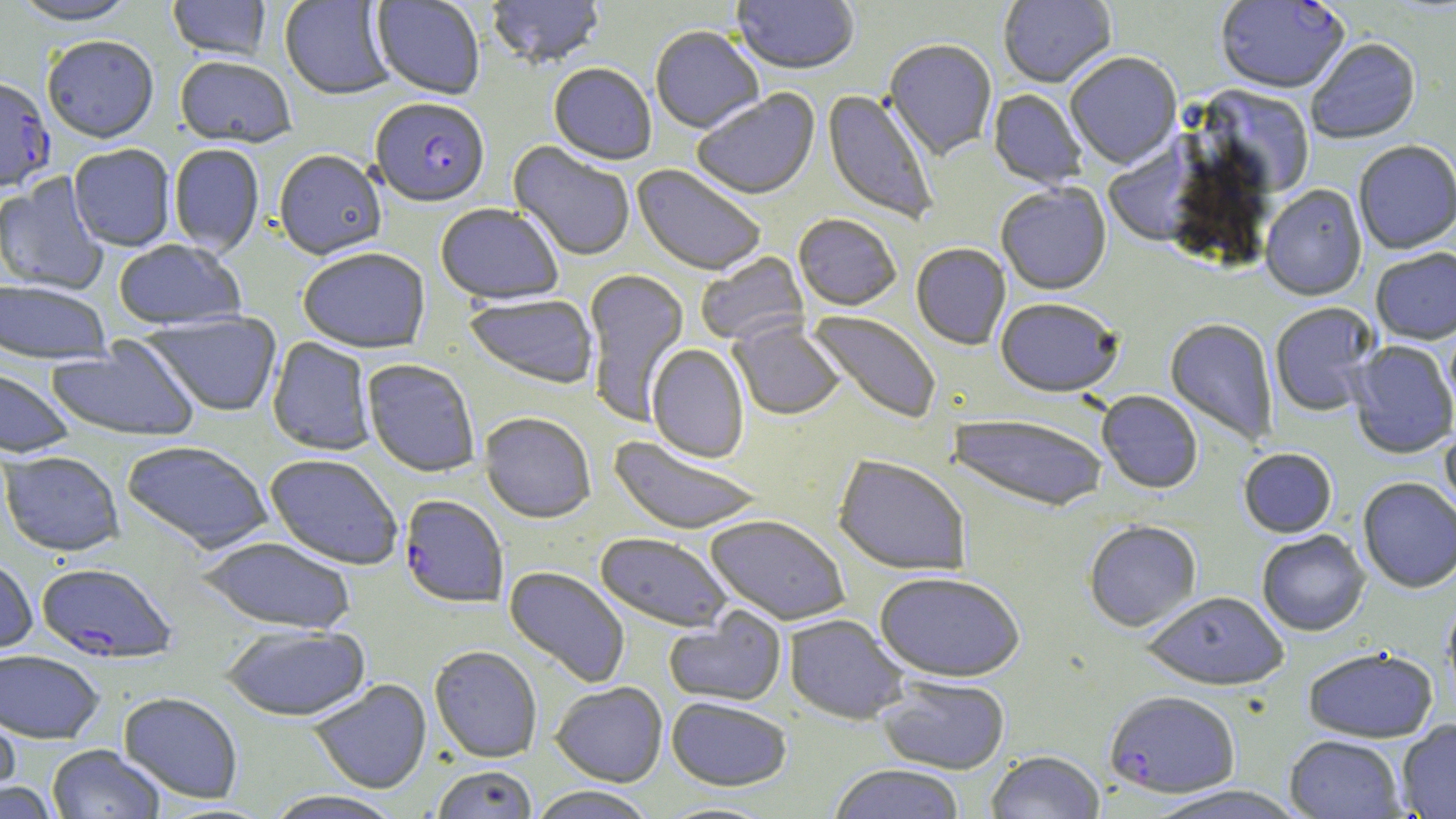

slide-level diagnosis = Plasmodium falciparum
field of view = one of a larger specimen
magnification = 1000x
preparation = thin blood film
uninfected red blood cell locations = approximate bounding boxes as [x1, y1, x2, y2] in pixels: [10, 0, 140, 29], [168, 0, 271, 62], [279, 0, 396, 102], [370, 0, 485, 101], [486, 0, 605, 71], [998, 0, 1116, 89], [731, 1, 860, 78], [650, 27, 764, 135], [43, 39, 159, 146], [1306, 39, 1421, 145], [883, 40, 997, 162], [1065, 54, 1182, 169], [175, 58, 296, 150], [548, 65, 657, 167], [1198, 86, 1315, 197], [692, 89, 821, 202], [822, 89, 939, 226], [988, 89, 1087, 189], [1103, 139, 1208, 248], [508, 142, 635, 262], [1353, 142, 1456, 254], [169, 145, 265, 258], [68, 146, 175, 252], [273, 151, 387, 262], [631, 165, 766, 277], [0, 174, 108, 296], [995, 183, 1112, 295], [1260, 185, 1367, 301], [435, 205, 563, 307], [793, 215, 901, 312], [113, 241, 246, 332], [911, 244, 1010, 350], [1370, 248, 1456, 345], [298, 250, 430, 355], [696, 252, 809, 347], [583, 269, 690, 427], [0, 281, 112, 366], [464, 294, 599, 390], [995, 297, 1124, 398], [1270, 303, 1381, 417], [142, 311, 284, 418], [806, 311, 942, 425], [1165, 319, 1278, 447], [730, 321, 845, 421], [47, 336, 199, 443], [266, 337, 376, 457], [1349, 341, 1456, 459], [647, 344, 749, 464], [362, 360, 480, 479], [0, 368, 75, 459], [1097, 391, 1202, 494], [480, 414, 596, 524], [948, 414, 1109, 512], [1440, 425, 1456, 524], [608, 436, 763, 536], [122, 441, 273, 556], [1238, 448, 1338, 538], [1, 452, 125, 558], [264, 455, 403, 571], [834, 455, 971, 576], [1357, 477, 1456, 593], [705, 515, 850, 626], [1083, 520, 1202, 632], [1257, 530, 1370, 636], [595, 532, 731, 632], [196, 538, 356, 636], [0, 557, 37, 657], [504, 566, 630, 688], [875, 571, 1025, 681], [1142, 591, 1288, 689], [1441, 597, 1456, 712], [664, 607, 787, 707], [784, 615, 909, 725], [222, 625, 371, 722], [1302, 646, 1438, 742], [429, 647, 542, 763], [0, 651, 104, 744], [878, 676, 1011, 774], [308, 679, 432, 794], [551, 682, 668, 787], [118, 693, 243, 804], [667, 697, 792, 791], [0, 710, 21, 806], [1396, 720, 1456, 818], [1284, 734, 1406, 818], [47, 745, 165, 819], [986, 750, 1105, 819], [828, 763, 965, 819], [431, 766, 538, 819], [0, 782, 59, 818], [1141, 784, 1309, 819], [527, 787, 656, 819], [264, 791, 404, 819], [655, 801, 780, 819]
image size = 1456×819 pixels
Plasmodium falciparum-infected red blood cell locations = approximate bounding boxes as [x1, y1, x2, y2] in pixels: [1216, 1, 1349, 95], [0, 80, 55, 195], [371, 100, 490, 210], [399, 496, 508, 610], [36, 563, 177, 665], [1104, 690, 1241, 797]
stain = May-Grünwald-Giemsa
modality = light microscopy